Report the malaria status of this cell.
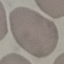

It is uninfected.

image type = cell patch, automatically extracted from a larger field of view and resized to 64 × 64 pixels
preparation = thin blood film
stain = Giemsa
capture = smartphone through the microscope eyepiece